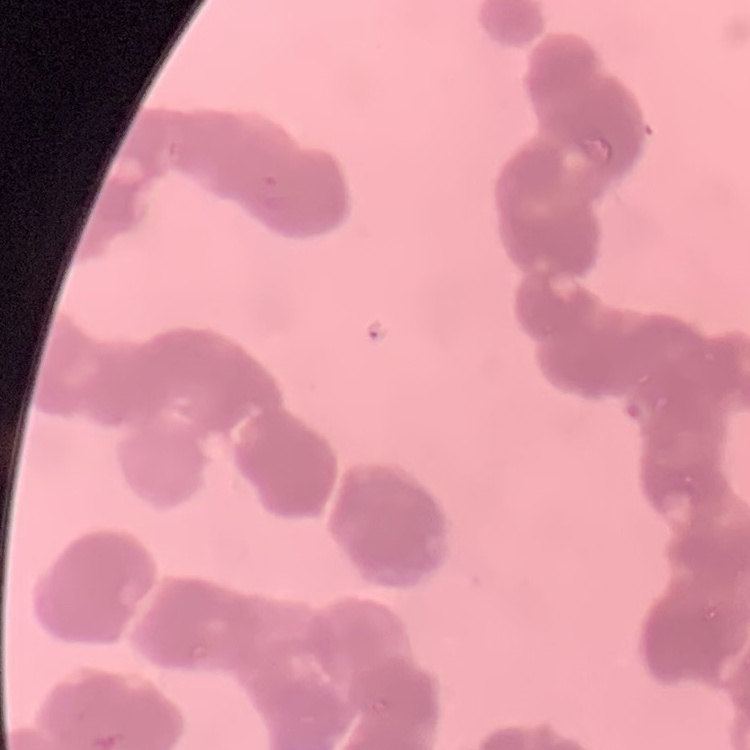

erythrocyte_morphology: rouleaux formation
stain: Field's or Giemsa
preparation: thin peripheral smear
image_type: square crop of a larger photomicrograph